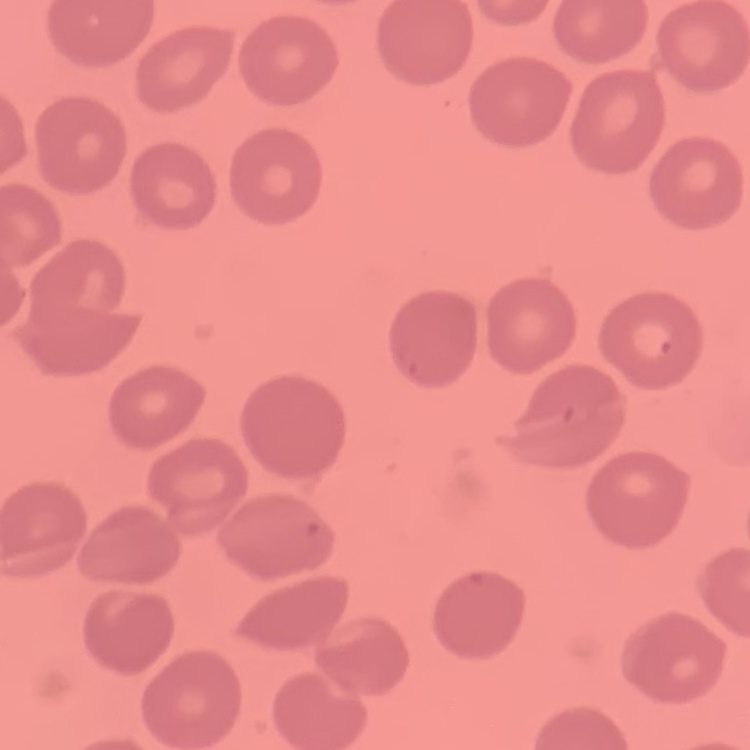

erythrocyte_morphology: no rouleaux formation
image_type: one tile cut from a larger photomicrograph
stain: Field's or Giemsa
preparation: thin blood smear